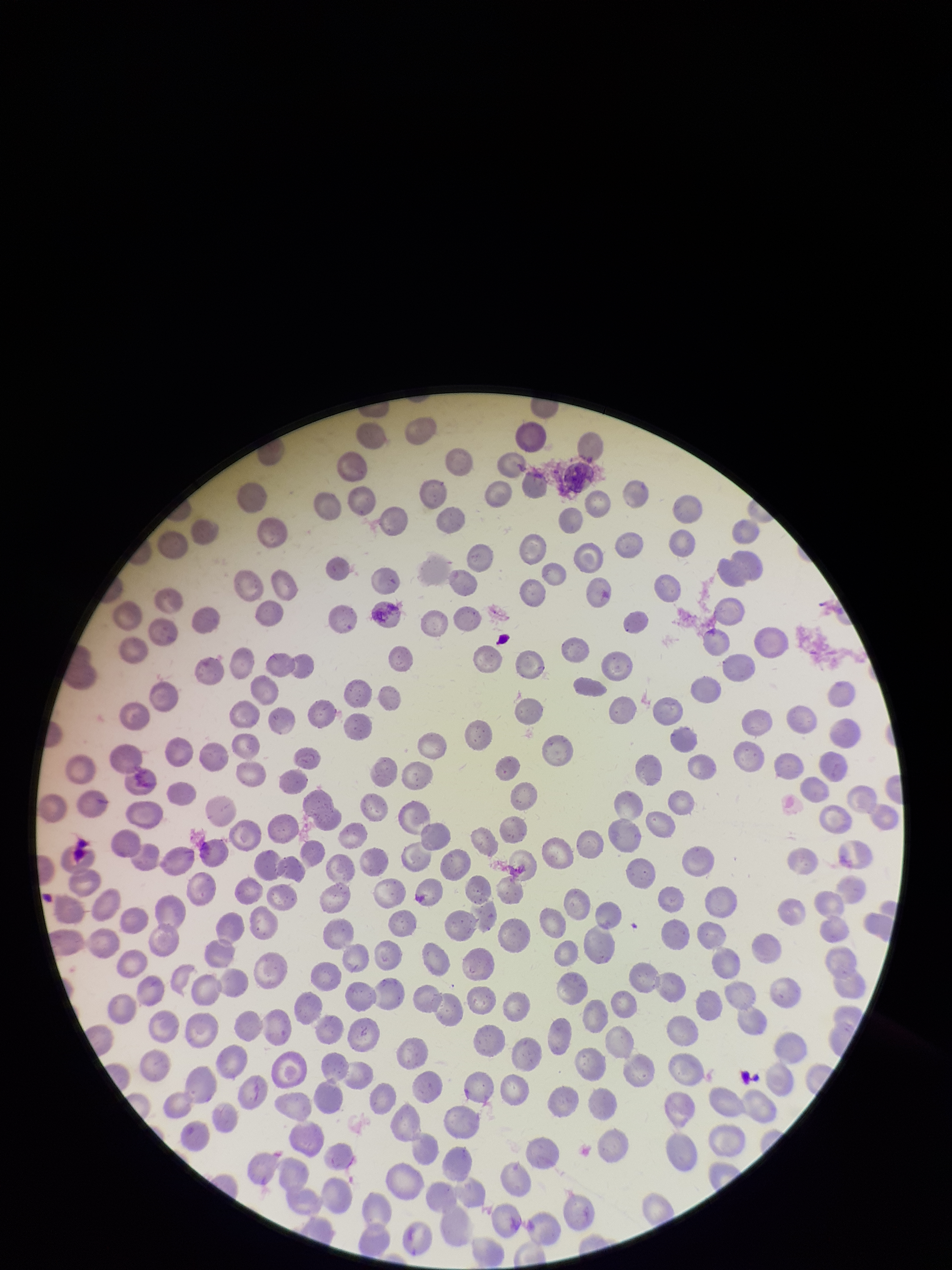

Summary:
  - Image size: 952×1270 pixels
  - Stain: Giemsa
  - Capture: smartphone photograph through the microscope eyepiece
  - Field of view: single
  - Parasitized red blood cell count: 0
  - Patient malaria status: negative
  - Preparation: thin blood smear
  - Red blood cell count: 275
  - Parasitized red blood cells: none detected